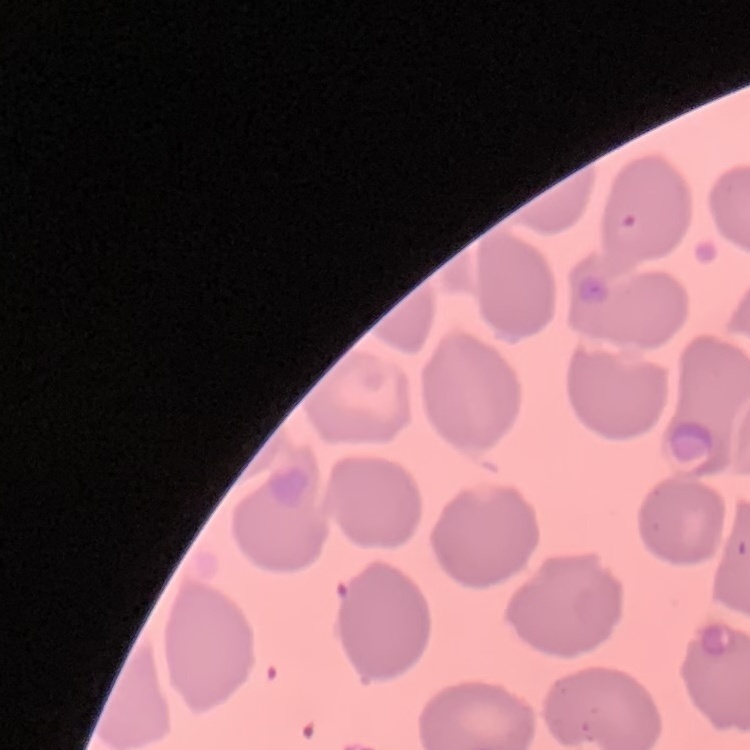

red blood cell morphology = no rouleaux formation
stain = Field's or Giemsa
image type = one tile cut from a larger photomicrograph
preparation = thin peripheral smear